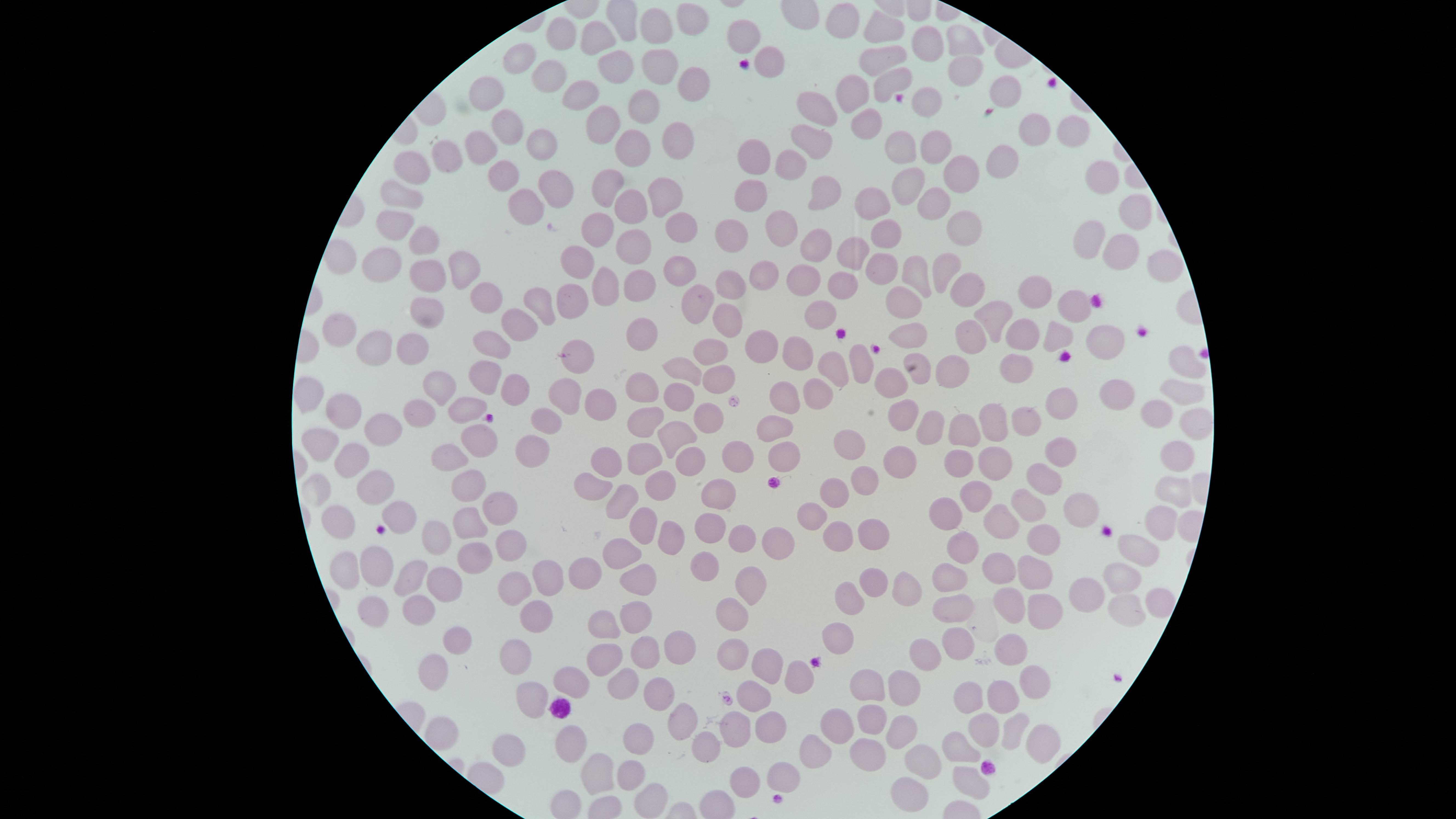

Approximate marker points, in pixels from the top-left corner.
Summary:
  - Uninfected red blood cells: (x=694, y=17), (x=844, y=18), (x=658, y=24), (x=881, y=25), (x=561, y=33), (x=743, y=34), (x=598, y=36), (x=961, y=39), (x=928, y=44), (x=521, y=56), (x=881, y=57), (x=617, y=60), (x=656, y=62), (x=769, y=64), (x=962, y=70), (x=547, y=77), (x=689, y=79), (x=890, y=80), (x=1003, y=87), (x=485, y=88), (x=582, y=91), (x=849, y=91), (x=645, y=104), (x=930, y=106), (x=818, y=109), (x=864, y=123), (x=602, y=124), (x=507, y=125), (x=1070, y=128), (x=1031, y=132), (x=813, y=138), (x=672, y=140), (x=540, y=142), (x=632, y=143), (x=478, y=145), (x=903, y=146), (x=938, y=146), (x=756, y=154), (x=442, y=156), (x=1006, y=158), (x=789, y=161), (x=412, y=170), (x=964, y=171), (x=500, y=177), (x=1100, y=177), (x=907, y=183), (x=554, y=187), (x=605, y=187), (x=822, y=187), (x=401, y=192), (x=665, y=192), (x=750, y=197), (x=930, y=197), (x=876, y=199), (x=520, y=203), (x=627, y=203), (x=1127, y=215), (x=390, y=219), (x=954, y=220), (x=595, y=226), (x=787, y=226), (x=677, y=227), (x=728, y=227), (x=888, y=235), (x=1087, y=235), (x=427, y=237), (x=633, y=242), (x=811, y=242), (x=849, y=252), (x=1111, y=252), (x=381, y=259), (x=580, y=261), (x=879, y=261), (x=1159, y=261), (x=464, y=265), (x=680, y=267), (x=944, y=267), (x=767, y=274), (x=423, y=275), (x=917, y=275), (x=805, y=281), (x=609, y=284), (x=734, y=284), (x=842, y=284), (x=636, y=286), (x=962, y=289), (x=1038, y=289), (x=571, y=297), (x=696, y=298), (x=493, y=299), (x=903, y=299), (x=430, y=302), (x=543, y=302), (x=1072, y=303), (x=820, y=313), (x=995, y=314), (x=726, y=318), (x=522, y=326), (x=339, y=328), (x=642, y=328), (x=912, y=332), (x=1016, y=336), (x=1051, y=336), (x=1103, y=338), (x=970, y=340), (x=413, y=342), (x=492, y=344), (x=762, y=344), (x=371, y=346), (x=716, y=352), (x=795, y=353), (x=858, y=359), (x=1180, y=360), (x=578, y=363), (x=956, y=364), (x=830, y=368), (x=1010, y=368), (x=687, y=370), (x=917, y=372), (x=492, y=373), (x=716, y=378), (x=897, y=380), (x=1180, y=384), (x=440, y=386), (x=642, y=386), (x=821, y=389), (x=514, y=391), (x=307, y=392), (x=567, y=392), (x=1118, y=395), (x=781, y=396), (x=601, y=399), (x=682, y=399), (x=1061, y=403), (x=417, y=406), (x=465, y=407), (x=703, y=410), (x=1153, y=413), (x=906, y=414), (x=1189, y=416), (x=385, y=418), (x=1024, y=418), (x=644, y=421), (x=778, y=422), (x=993, y=422), (x=540, y=424), (x=929, y=427), (x=967, y=430), (x=674, y=433), (x=478, y=435), (x=321, y=443), (x=857, y=445), (x=531, y=449), (x=1066, y=453), (x=742, y=454), (x=783, y=454), (x=450, y=457), (x=605, y=458), (x=642, y=458), (x=691, y=459), (x=1177, y=460), (x=965, y=461), (x=1000, y=461), (x=345, y=463), (x=901, y=463), (x=1047, y=477), (x=870, y=479), (x=589, y=480), (x=658, y=481), (x=378, y=487), (x=464, y=487), (x=1174, y=492), (x=716, y=493), (x=837, y=494), (x=977, y=496), (x=619, y=501), (x=1025, y=506), (x=494, y=507), (x=946, y=509), (x=1083, y=511), (x=399, y=515), (x=814, y=515), (x=467, y=521), (x=1159, y=521), (x=334, y=523), (x=642, y=523), (x=1002, y=525), (x=709, y=526), (x=440, y=532), (x=838, y=533), (x=742, y=534), (x=876, y=534), (x=1047, y=539), (x=503, y=541), (x=668, y=541), (x=773, y=542), (x=1139, y=544), (x=964, y=547), (x=615, y=552), (x=475, y=554), (x=378, y=566), (x=345, y=568), (x=711, y=570), (x=1004, y=571), (x=582, y=572), (x=1042, y=573), (x=634, y=575), (x=403, y=580), (x=753, y=581), (x=1121, y=581), (x=538, y=582), (x=864, y=584), (x=947, y=586), (x=439, y=587), (x=503, y=589), (x=901, y=590), (x=1085, y=595), (x=1155, y=601), (x=846, y=602), (x=417, y=609), (x=1010, y=610), (x=1127, y=610), (x=372, y=611), (x=1039, y=611), (x=957, y=612), (x=734, y=613), (x=636, y=615), (x=607, y=620), (x=527, y=621), (x=837, y=631), (x=456, y=638), (x=953, y=642), (x=1009, y=649), (x=645, y=653), (x=675, y=653), (x=732, y=654), (x=508, y=656), (x=605, y=662), (x=914, y=664), (x=762, y=666), (x=424, y=670), (x=570, y=678), (x=801, y=682), (x=1027, y=683), (x=619, y=684), (x=900, y=689), (x=533, y=693), (x=863, y=695), (x=759, y=697), (x=998, y=697), (x=654, y=698), (x=971, y=701), (x=675, y=720), (x=870, y=724), (x=768, y=725), (x=841, y=727), (x=440, y=731), (x=982, y=731), (x=735, y=732), (x=893, y=733), (x=1017, y=733), (x=1036, y=740), (x=635, y=742), (x=702, y=746), (x=957, y=748), (x=568, y=750), (x=816, y=752), (x=504, y=753), (x=868, y=758), (x=930, y=768), (x=626, y=771), (x=777, y=774), (x=590, y=776), (x=734, y=779), (x=966, y=783), (x=904, y=793), (x=649, y=795)
  - Presence: no malaria parasites identified
  - Field of view: single
  - Capture: smartphone photograph through the microscope eyepiece
  - Stain: Giemsa
  - Image size: 1456×819 pixels
  - Preparation: thin blood film
  - Visible region: circular